Classify this cell by malaria status.
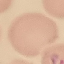

Parasitized.

Cell patch, automatically extracted from a larger field of view and resized to 64 × 64 pixels. Giemsa-stained preparation. Photographed with a smartphone camera at the microscope eyepiece. Thin blood film.